Name the parasite shown.
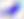
Toxoplasma gondii.

Photomicrograph. 400x magnification.